Assess for malaria.
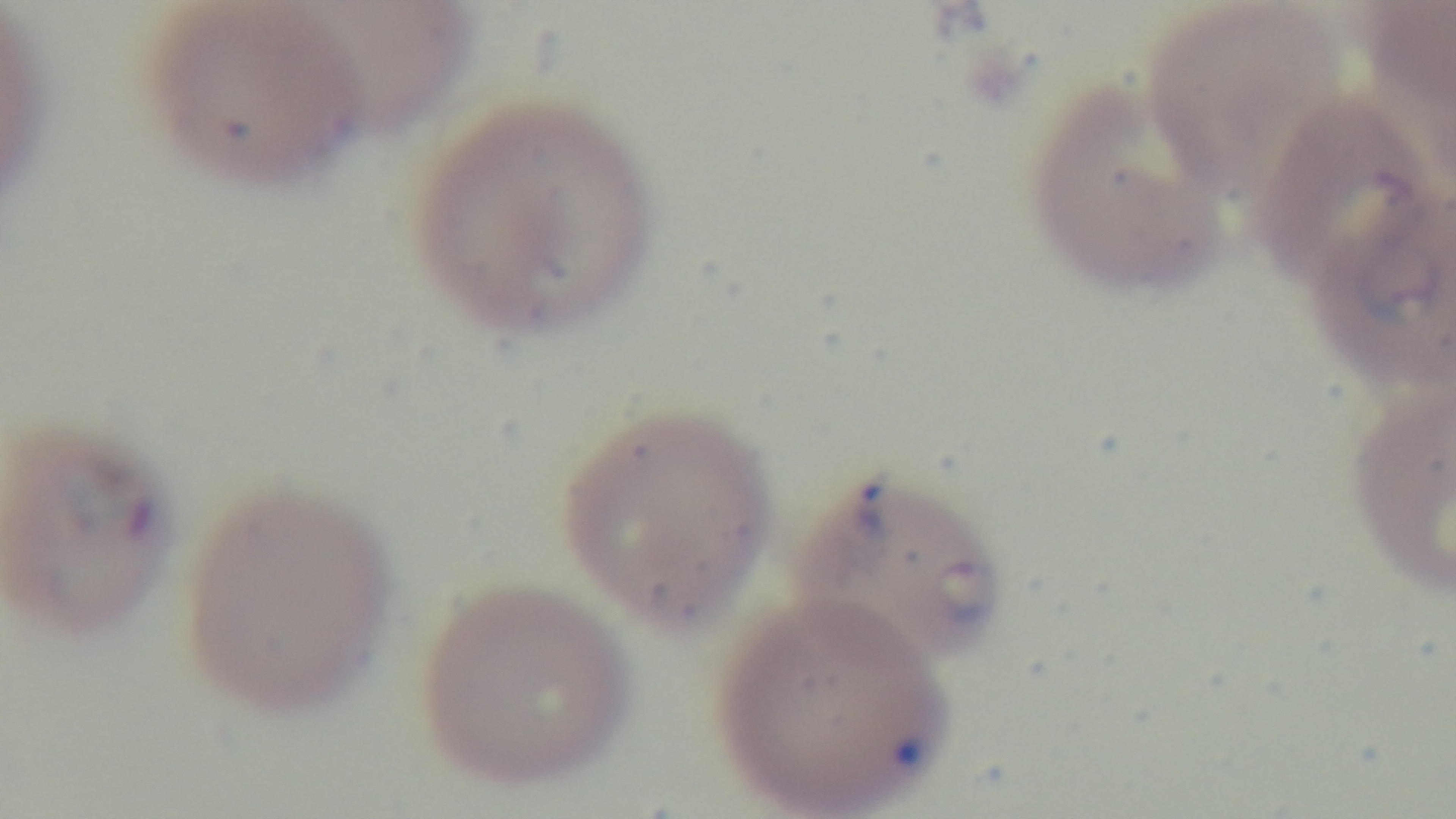
It is infected.

Preparation: thin smear. Captured with a mounted 4K digital camera. Light microscopy. Giemsa-stained. Oil-immersion objective, 100x. One field from the slide.